Classify this cell by malaria status.
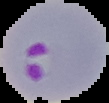
It is parasitized.

Segmented cell region on a black background. Image is 109×103 pixels. From a thin blood smear.